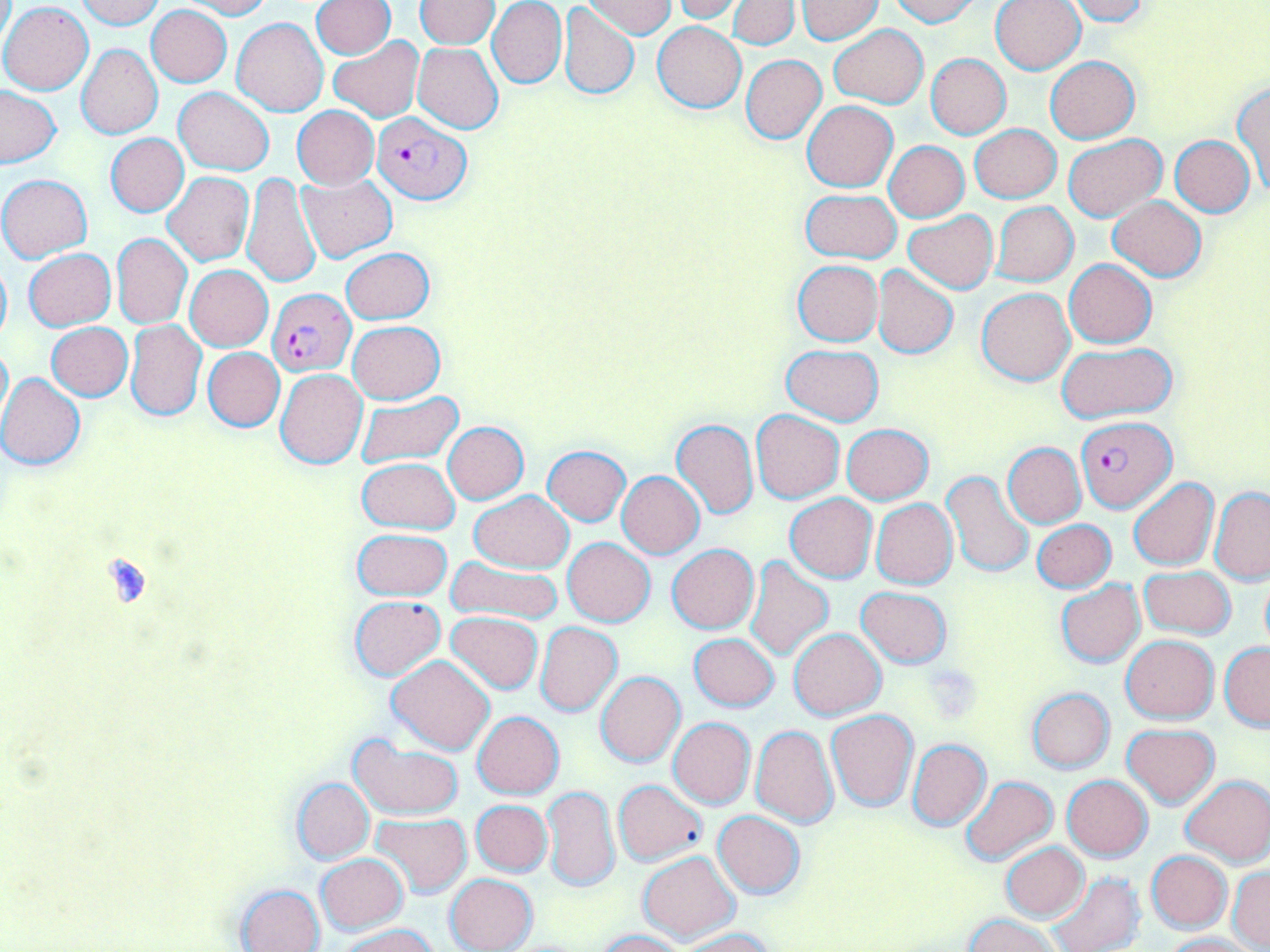
Summary:
  - Coordinate format: approximate bounding boxes as (x1, y1, x2, y2) in pixels
  - Plasmodium falciparum-infected red blood cell locations: (372, 111, 471, 205), (268, 289, 355, 375), (1076, 415, 1176, 511)
  - Uninfected red blood cell locations: (75, 0, 164, 30), (180, 0, 272, 19), (416, 0, 500, 49), (488, 0, 567, 89), (582, 0, 675, 38), (728, 0, 800, 50), (796, 0, 883, 44), (888, 0, 980, 26), (991, 0, 1085, 73), (1062, 0, 1150, 24), (311, 1, 395, 59), (674, 1, 745, 23), (1, 3, 93, 94), (557, 4, 639, 100), (147, 5, 232, 87), (233, 18, 329, 117), (652, 21, 747, 113), (829, 24, 927, 108), (329, 36, 425, 122), (412, 43, 503, 135), (76, 44, 163, 139), (926, 53, 1010, 138), (742, 55, 826, 143), (1045, 56, 1140, 143), (1234, 83, 1270, 193), (0, 85, 62, 168), (174, 87, 274, 175), (803, 101, 898, 192), (293, 106, 379, 189), (970, 124, 1061, 203), (105, 132, 187, 217), (1063, 134, 1166, 221), (1170, 135, 1254, 217), (884, 140, 969, 222), (242, 172, 320, 289), (163, 173, 254, 266), (295, 174, 397, 263), (0, 175, 91, 262), (800, 188, 902, 263), (1109, 196, 1206, 281), (991, 202, 1079, 286), (902, 211, 997, 293), (112, 234, 191, 329), (341, 247, 433, 324), (24, 248, 116, 330), (0, 252, 11, 350), (1065, 259, 1156, 348), (793, 260, 883, 345), (872, 264, 959, 359), (185, 265, 272, 351), (977, 288, 1075, 385), (127, 320, 206, 420), (348, 322, 445, 403), (46, 323, 132, 400), (0, 341, 12, 426), (780, 344, 885, 426), (1056, 344, 1178, 423), (203, 347, 284, 431), (276, 368, 368, 469), (0, 372, 86, 469), (356, 391, 462, 467), (751, 410, 844, 502), (671, 419, 759, 521), (441, 422, 529, 504), (841, 424, 933, 504), (1002, 443, 1086, 528), (541, 446, 631, 526), (358, 457, 460, 535), (942, 470, 1033, 577), (617, 471, 704, 558), (1128, 478, 1218, 571), (1210, 487, 1270, 583), (469, 490, 573, 574), (786, 494, 877, 582), (872, 499, 957, 589), (1033, 519, 1115, 592), (353, 528, 452, 600), (563, 537, 655, 626), (668, 544, 759, 633), (445, 557, 564, 625), (744, 557, 834, 661), (1140, 566, 1236, 639), (1260, 574, 1270, 653), (1056, 580, 1143, 667), (856, 587, 953, 667), (350, 595, 445, 679), (446, 611, 542, 694), (535, 622, 623, 717), (789, 627, 886, 720), (689, 633, 780, 712), (1122, 634, 1218, 723), (1220, 643, 1270, 730), (386, 656, 495, 755), (596, 672, 685, 767), (1027, 687, 1115, 773), (826, 710, 918, 811), (473, 711, 564, 798), (668, 717, 755, 808), (750, 724, 839, 828), (1122, 724, 1219, 807), (347, 736, 464, 820), (907, 739, 991, 831), (1061, 775, 1153, 862), (1181, 775, 1270, 867), (960, 776, 1057, 865), (292, 778, 374, 865), (613, 780, 707, 866), (542, 786, 620, 893), (471, 800, 552, 876), (712, 810, 806, 898), (371, 813, 472, 897), (999, 842, 1089, 922), (638, 851, 739, 944), (1147, 851, 1232, 933), (316, 852, 408, 933), (1228, 866, 1270, 950), (1047, 871, 1143, 952), (444, 873, 539, 952), (235, 883, 326, 952), (964, 914, 1063, 952), (340, 924, 440, 952), (678, 928, 776, 952), (595, 929, 686, 952), (1163, 932, 1258, 952)
  - Platelet locations: (921, 663, 981, 722)
  - Slide-level diagnosis: Plasmodium falciparum
  - Preparation: thin blood film
  - Modality: optical microscopy
  - Field of view: single
  - Stain: May-Grünwald-Giemsa
  - Magnification: 1000x
  - Image size: 1270×952 pixels